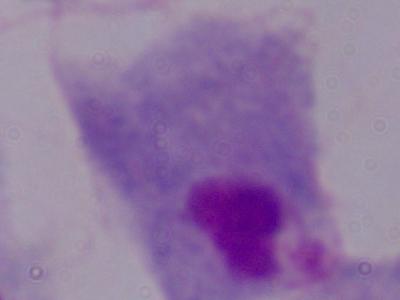
A trichomonad is seen. 1000x magnification. Micrograph.